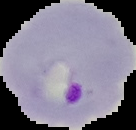

Summary:
  - Preparation: thin blood film
  - Image type: segmented cell region with the area outside set to black
  - Result: malaria parasites identified
  - Image size: 136×130 pixels